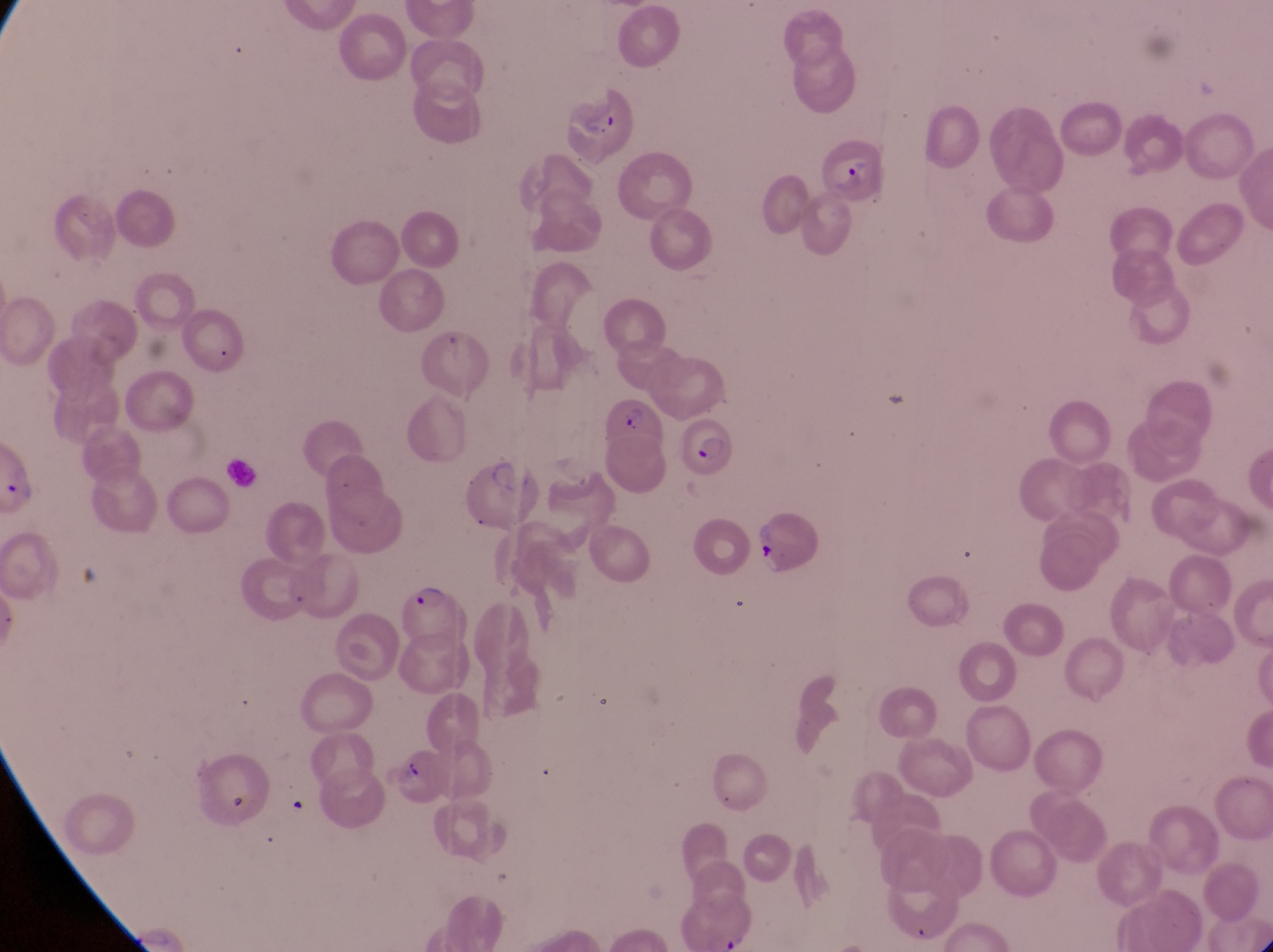 Approximate bounding boxes as (left, top, right, bottom) in pixels. Artifact (platelet-like body, stain precipitate, or debris) locations: (394, 757, 427, 789). Parasitised red blood cell locations: (567, 87, 641, 169), (814, 137, 888, 204), (602, 392, 660, 449), (684, 417, 737, 475), (756, 512, 828, 570), (400, 584, 470, 656). Trophozoite locations: (2, 469, 42, 506). Single field of view. Magnification of 1000x. Thin blood film. Collected in Uganda. Photographed through the eyepiece of an Olympus CX-23 microscope with a smartphone camera. Image is 1273×952 pixels.